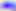

magnification: 400x
identification: Toxoplasma gondii
modality: micrograph